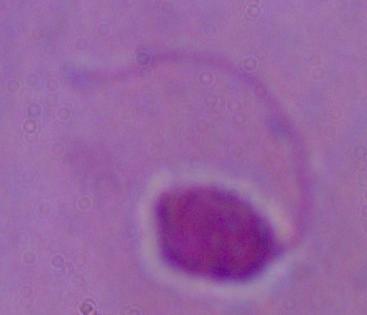

{
  "magnification": "1000x",
  "modality": "micrograph",
  "identification": "Leishmania"
}